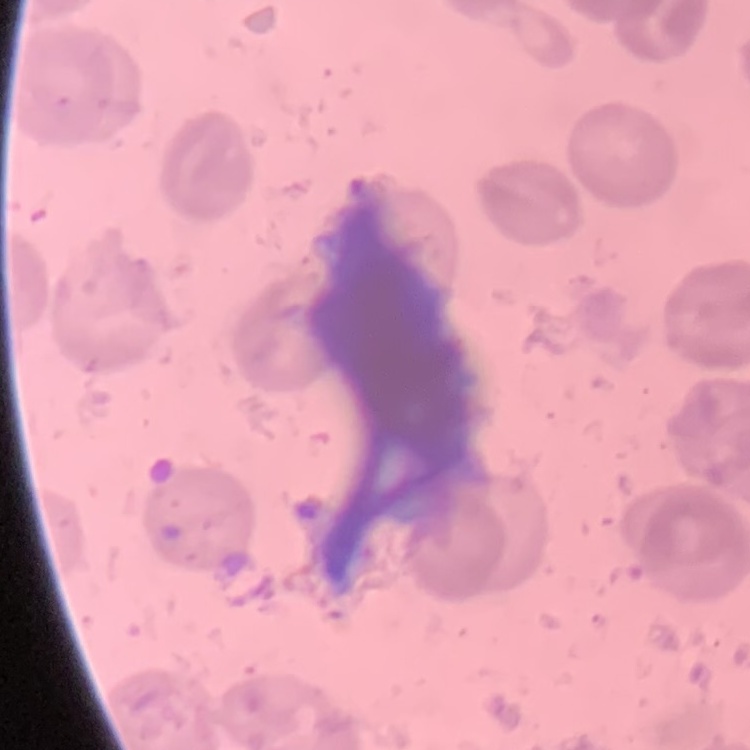 The red blood cells show no rouleaux formation. Thin peripheral smear. Field's or Giemsa stain. Square crop of a larger photomicrograph.